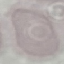
Summary:
  - Malaria status: uninfected
  - Image type: cell patch, automatically extracted from a larger field of view and resized to 64 × 64 pixels
  - Preparation: thin blood smear
  - Capture: smartphone camera at the microscope eyepiece
  - Stain: Giemsa